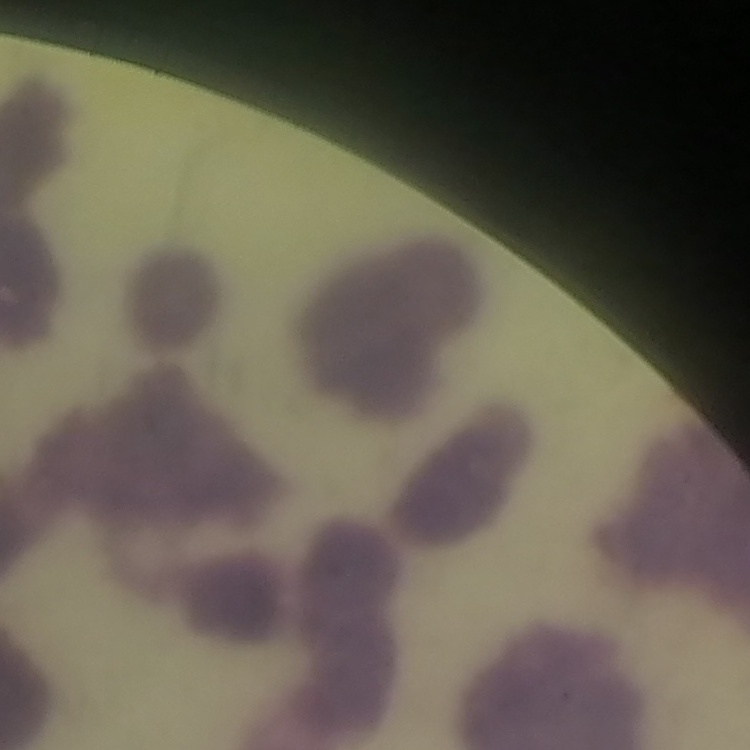

Summary:
  - Erythrocyte morphology: rouleaux formation
  - Stain: Field's or Giemsa
  - Preparation: thin blood film
  - Image type: square crop of a larger photomicrograph